Give the location of every parasitized red blood cell.
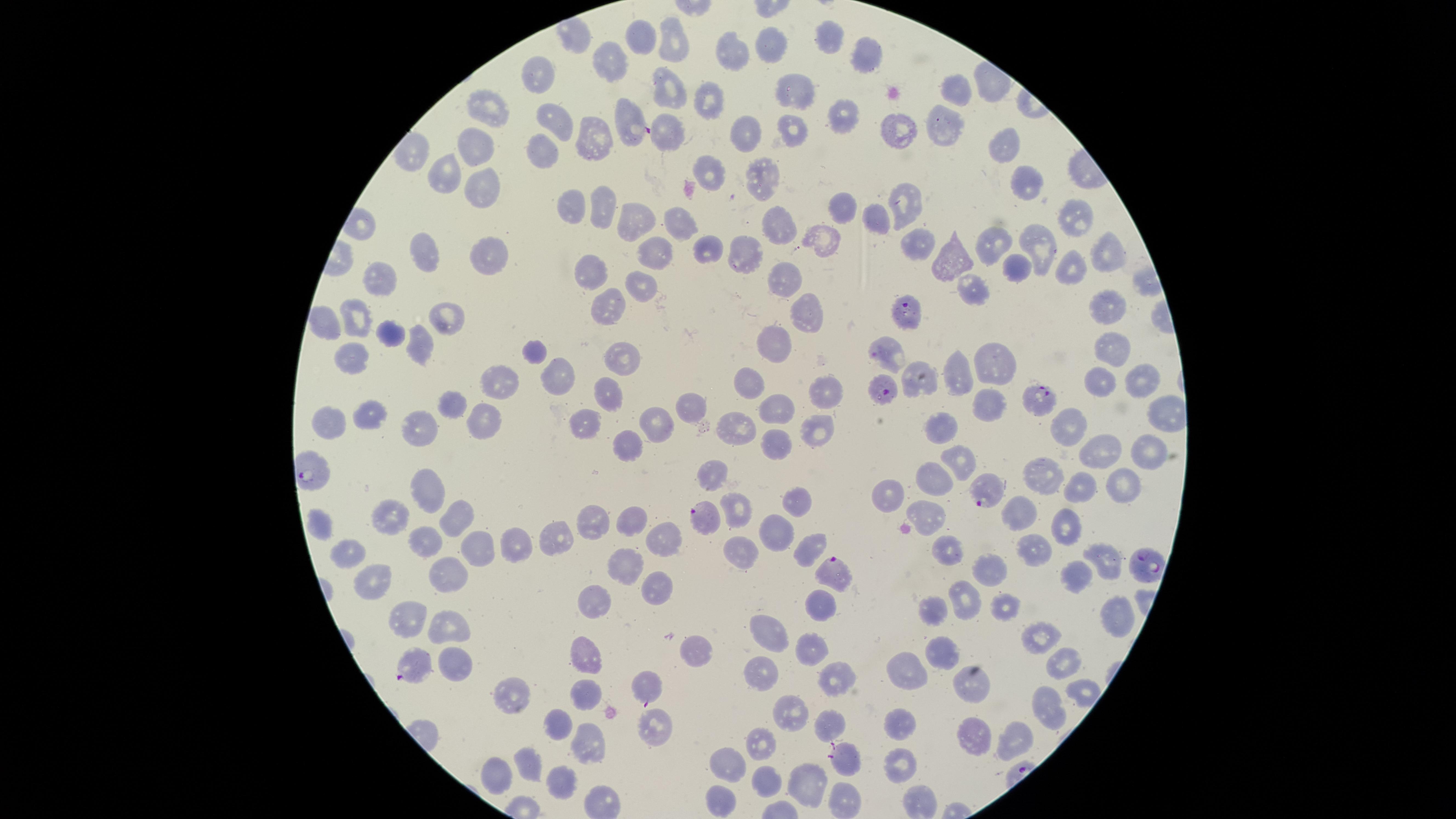
Approximate marker points as [x, y] in pixels.
Parasitized red blood cells: [629, 124], [907, 313], [883, 356], [883, 387], [1042, 400], [981, 492], [704, 522], [1139, 568], [837, 570], [410, 664], [647, 689], [841, 754].

Approximate marker points as [x, y] in pixels. Uninfected red blood cells: [824, 37], [773, 50], [729, 54], [866, 56], [603, 65], [543, 77], [949, 88], [798, 90], [712, 103], [485, 115], [844, 115], [937, 123], [555, 125], [893, 127], [794, 130], [662, 133], [751, 133], [590, 139], [1006, 142], [472, 149], [542, 153], [708, 173], [444, 174], [762, 175], [1022, 180], [483, 191], [596, 207], [844, 207], [903, 207], [575, 208], [1073, 212], [871, 218], [776, 224], [682, 226], [634, 228], [825, 235], [993, 245], [1037, 246], [915, 247], [706, 249], [747, 252], [656, 255], [955, 255], [1104, 255], [491, 260], [421, 262], [1073, 266], [1015, 269], [591, 270], [789, 277], [386, 285], [968, 287], [641, 288], [601, 307], [1107, 309], [810, 312], [355, 318], [446, 318], [326, 328], [388, 335], [426, 340], [1116, 346], [777, 348], [537, 358], [618, 358], [350, 360], [995, 367], [956, 377], [509, 379], [552, 379], [917, 379], [1142, 380], [1106, 383], [748, 387], [820, 388], [607, 389], [452, 397], [990, 405], [681, 407], [775, 408], [368, 412], [484, 421], [423, 422], [330, 423], [591, 424], [656, 424], [1066, 425], [820, 428], [943, 428], [738, 429], [629, 439], [1143, 443], [770, 447], [1095, 450], [957, 456], [1048, 476], [933, 482], [1126, 485], [1085, 487], [429, 489], [886, 494], [798, 501], [737, 503], [1020, 510], [926, 512], [390, 513], [628, 516], [453, 518], [319, 519], [593, 521], [1063, 524], [771, 533], [554, 541], [663, 542], [428, 544], [522, 547], [808, 547], [482, 549], [954, 549], [1033, 549], [739, 552], [1101, 555], [352, 557], [621, 566], [446, 571], [992, 573], [1076, 576], [379, 579], [657, 586], [968, 599], [599, 603], [820, 604], [1009, 605], [935, 613], [405, 617], [1112, 619], [443, 627], [767, 627], [1042, 635], [813, 642], [947, 651], [692, 654], [585, 656], [1067, 661], [453, 663], [916, 668], [756, 672], [835, 683], [974, 685], [581, 693], [520, 696], [1042, 713], [787, 715], [550, 725], [899, 725], [656, 726], [826, 726], [968, 735], [1006, 738], [582, 746], [759, 746], [903, 759], [729, 761], [527, 766], [493, 778], [560, 782], [761, 784], [805, 786], [722, 802]. Giemsa stain. Circular visible region. Thin blood smear. Photographed with a smartphone camera through the microscope eyepiece. Single field of view. Image is 1456×819 pixels. Species: Plasmodium falciparum.